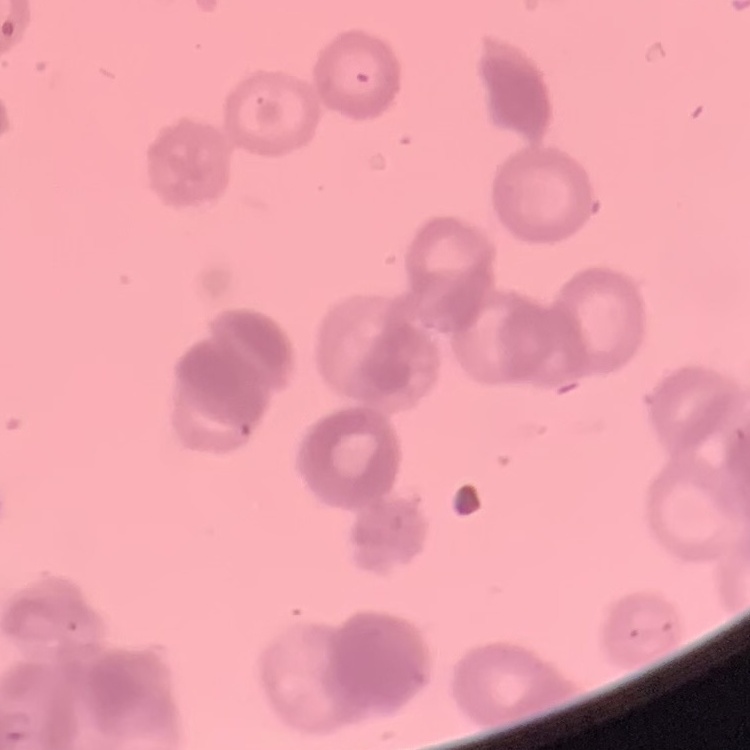 The erythrocytes show rouleaux formation. One tile cut from a larger photomicrograph. Field's or Giemsa stain. Thin peripheral smear.